Describe the morphology of the red blood cells.
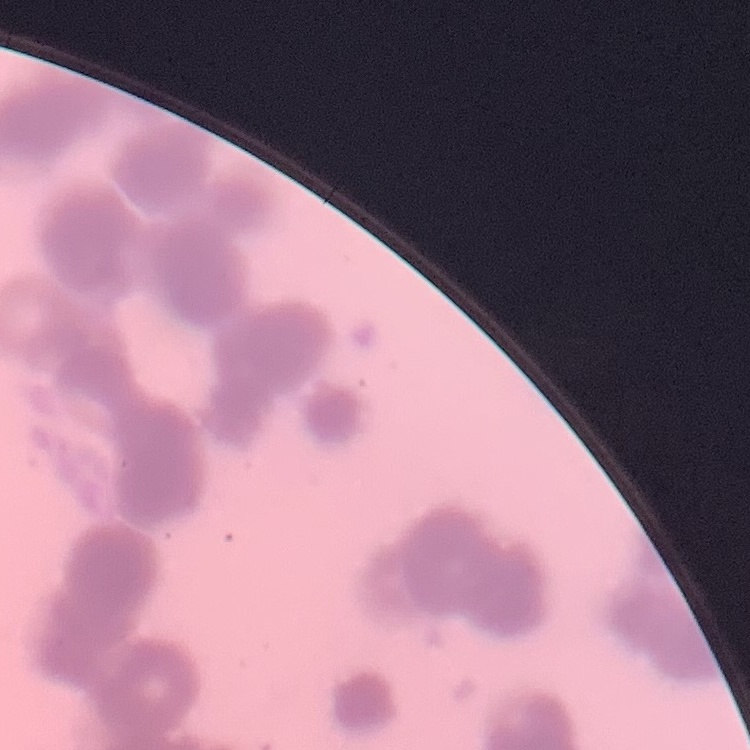

Rouleaux formation.

Thin blood smear. Field's or Giemsa stain. One tile cut from a larger photomicrograph.